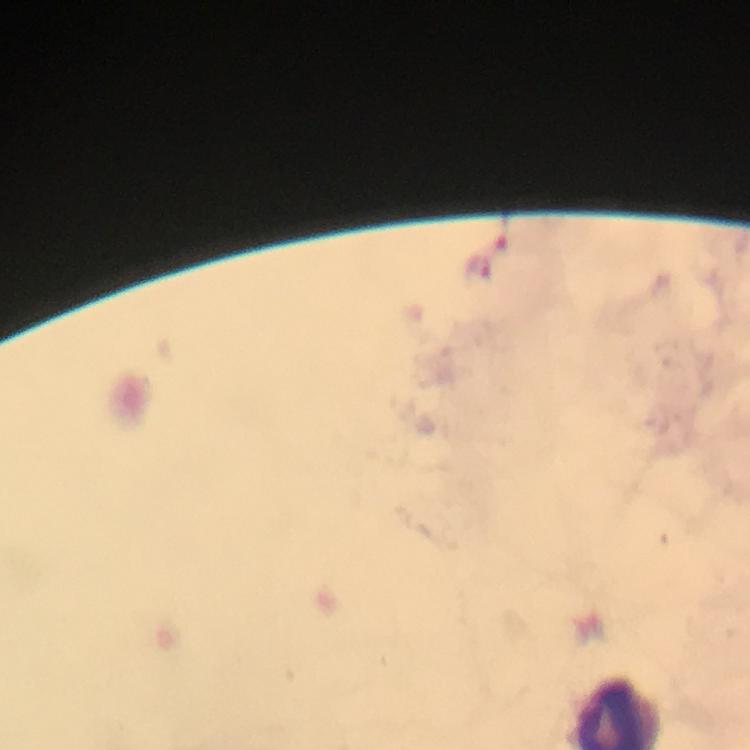
Approximate centers as {x, y} in pixels.
Summary:
  - Plasmodium parasite locations: {476, 268}
  - Capture: smartphone camera through the microscope
  - Image size: 750×750 pixels
  - Magnification: 100x
  - Context: from a malaria diagnostic workup
  - Immersion oil: used
  - Stain: Giemsa
  - Cropped from: a single field of view
  - Preparation: thick blood film